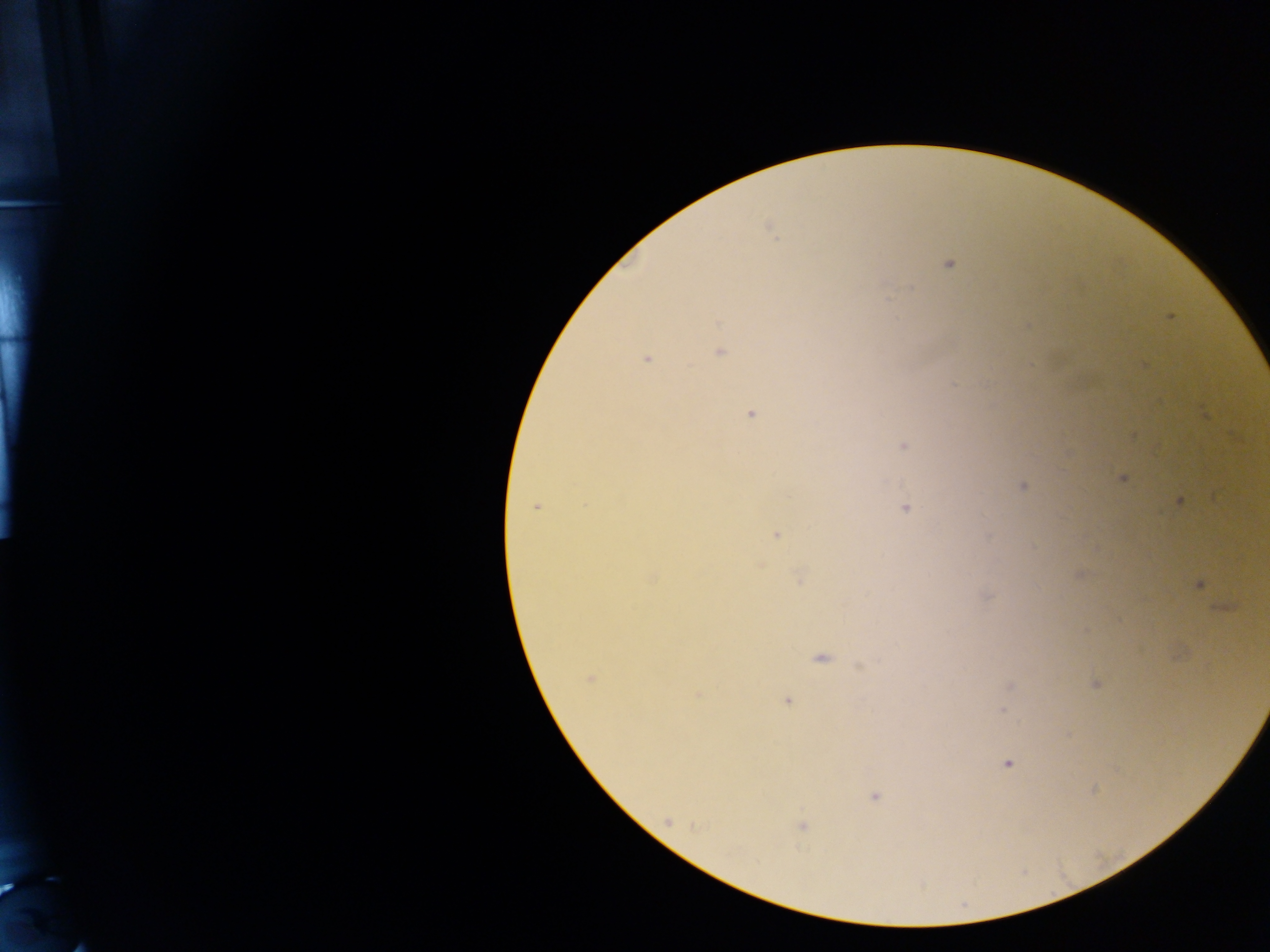
preparation: thick blood film
capture: mobile-phone photograph through a microscope
field_of_view: single
image_size: 1270×952 pixels
malaria_parasite_locations: 'approximate centers as (x, y) in pixels: (770, 230), (949, 263), (1170, 318), (1028, 326), (720, 352), (646, 359), (1145, 366), (750, 414), (1132, 437), (903, 446), (1123, 478), (1023, 486), (1178, 500), (536, 507), (906, 508), (776, 535), (1081, 574), (798, 578), (1200, 585), (987, 595), (821, 659), (860, 667), (590, 679), (1096, 684), (1011, 686), (697, 694), (787, 701), (1003, 710), (1007, 763), (1093, 790), (875, 797), (668, 821), (802, 827)'
country: Ghana